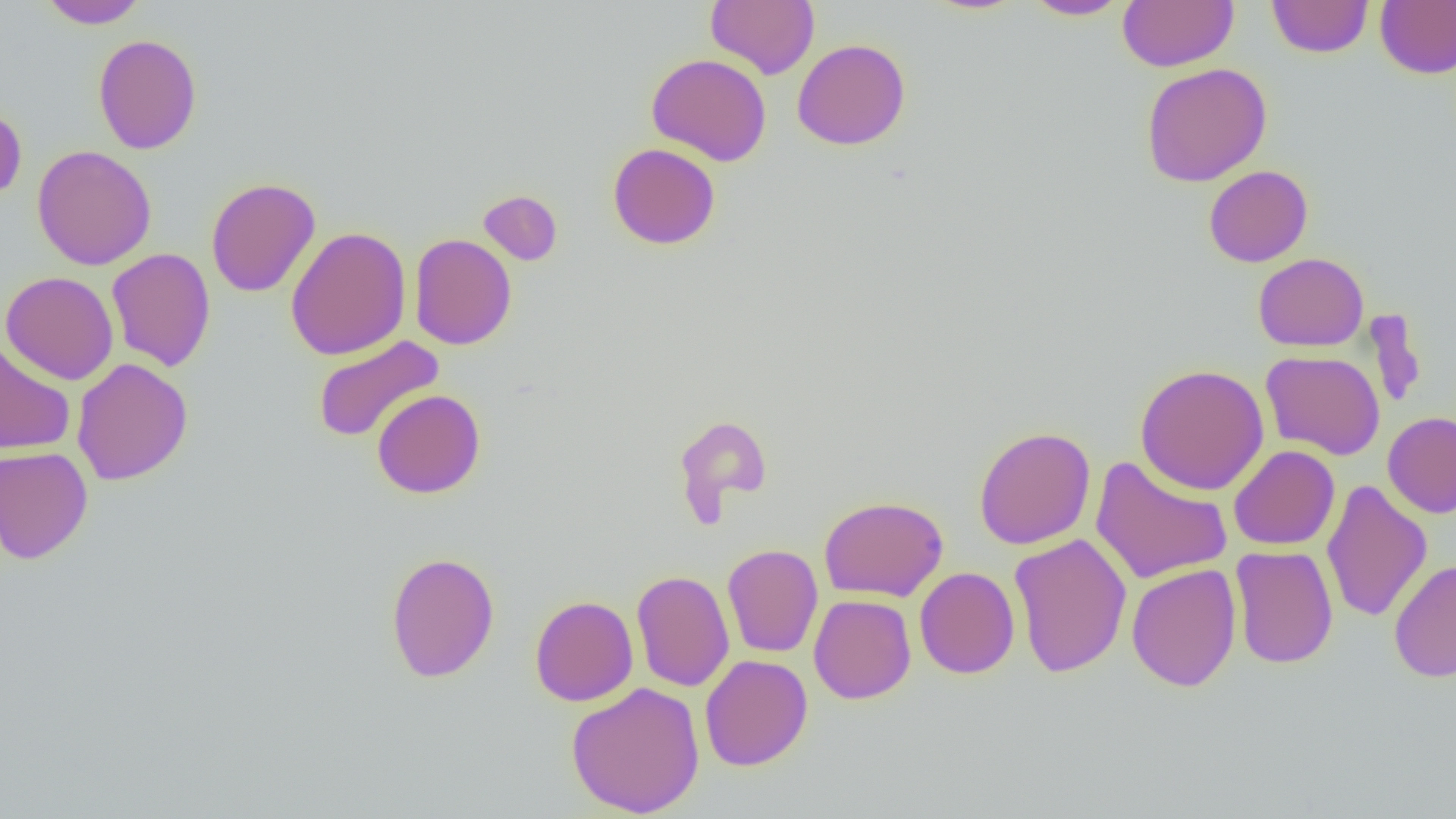 Approximate bounding boxes as (x1, y1, x2, y2) in pixels. Uninfected red blood cell locations: (39, 0, 148, 29), (705, 0, 819, 79), (1022, 0, 1132, 20), (1117, 0, 1238, 73), (1266, 0, 1374, 58), (1375, 0, 1456, 79), (93, 34, 202, 154), (791, 38, 911, 151), (646, 53, 772, 166), (1140, 63, 1272, 187), (0, 104, 27, 204), (607, 143, 720, 249), (32, 145, 157, 270), (1203, 165, 1313, 267), (206, 177, 321, 298), (478, 190, 562, 266), (285, 226, 411, 360), (409, 233, 517, 350), (106, 248, 216, 372), (1253, 253, 1369, 352), (1, 271, 119, 385), (1365, 310, 1427, 410), (312, 335, 445, 444), (0, 340, 75, 454), (1261, 350, 1386, 460), (72, 358, 192, 486), (1135, 363, 1269, 495), (372, 389, 486, 499), (1383, 411, 1456, 518), (673, 414, 772, 521), (973, 426, 1096, 550), (1228, 445, 1340, 550), (0, 446, 93, 564), (1089, 455, 1234, 585), (1321, 479, 1432, 623), (819, 495, 949, 602), (1008, 533, 1132, 678), (722, 543, 823, 658), (1229, 544, 1338, 669), (385, 551, 500, 683), (1389, 558, 1456, 683), (1126, 562, 1241, 693), (915, 567, 1019, 679), (631, 570, 735, 692), (808, 594, 916, 704), (529, 595, 638, 706), (699, 653, 813, 771), (566, 681, 705, 818). Slide-level diagnosis: negative for blood parasites. Thin blood smear. Image is 1456×819 pixels. 1000x magnification. Optical microscopy. Single field of view.